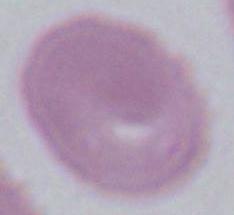
identification: erythrocyte
magnification: 1000x
modality: photomicrograph